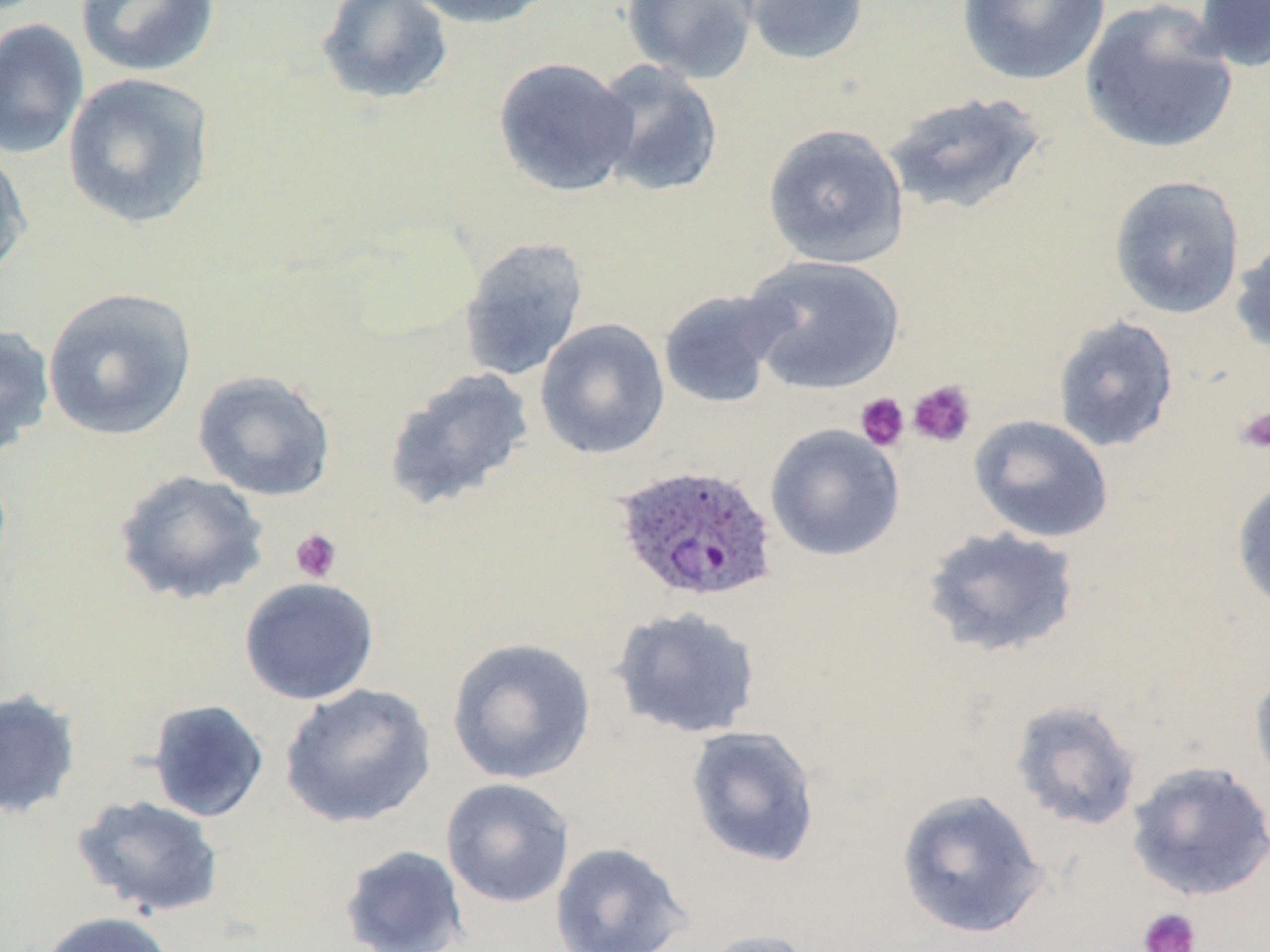
Summary:
  - Coordinate format: approximate bounding boxes as [x1, y1, x2, y2] in pixels
  - Uninfected red blood cell locations: [75, 0, 221, 78], [315, 0, 454, 106], [403, 0, 558, 30], [622, 0, 759, 83], [735, 0, 871, 66], [957, 0, 1112, 86], [1192, 0, 1270, 73], [1080, 1, 1239, 156], [0, 19, 89, 160], [493, 57, 638, 197], [590, 59, 724, 198], [62, 72, 217, 229], [882, 91, 1047, 217], [762, 123, 909, 269], [0, 143, 32, 282], [1109, 175, 1245, 319], [1230, 231, 1270, 359], [458, 237, 589, 382], [741, 255, 906, 395], [42, 286, 197, 441], [658, 289, 790, 410], [1052, 315, 1179, 453], [535, 318, 670, 459], [0, 323, 55, 461], [382, 367, 535, 512], [192, 369, 337, 502], [969, 414, 1114, 543], [764, 423, 905, 562], [113, 468, 270, 606], [1231, 477, 1270, 615], [921, 525, 1083, 659], [238, 576, 380, 705], [609, 605, 763, 740], [445, 637, 596, 785], [1249, 665, 1270, 798], [279, 683, 436, 829], [0, 688, 82, 819], [147, 698, 270, 823], [1009, 698, 1143, 833], [685, 725, 821, 868], [1126, 761, 1270, 901], [440, 778, 575, 908], [895, 788, 1050, 941], [71, 794, 225, 918], [549, 841, 694, 952], [339, 844, 470, 951], [37, 911, 180, 952], [695, 928, 821, 952]
  - Plasmodium ovale-infected red blood cell locations: [612, 464, 779, 605]
  - Platelet locations: [907, 379, 977, 448], [855, 392, 910, 451], [1236, 407, 1270, 454], [290, 528, 342, 583], [1137, 907, 1201, 952]
  - Slide-level diagnosis: Plasmodium ovale
  - Magnification: 1000x
  - Image size: 1270×952 pixels
  - Modality: light microscopy
  - Preparation: thin blood film
  - Stain: May-Grünwald-Giemsa
  - Field of view: single